Classify this cell by malaria status.
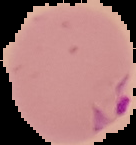
Parasitized.

image type = cell region segmented out of the field of view; surrounding area masked to black
preparation = thin blood film
image size = 136×145 pixels